Name the parasite shown.
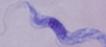
A trypanosome.

Captured at 1000x magnification. Micrograph.